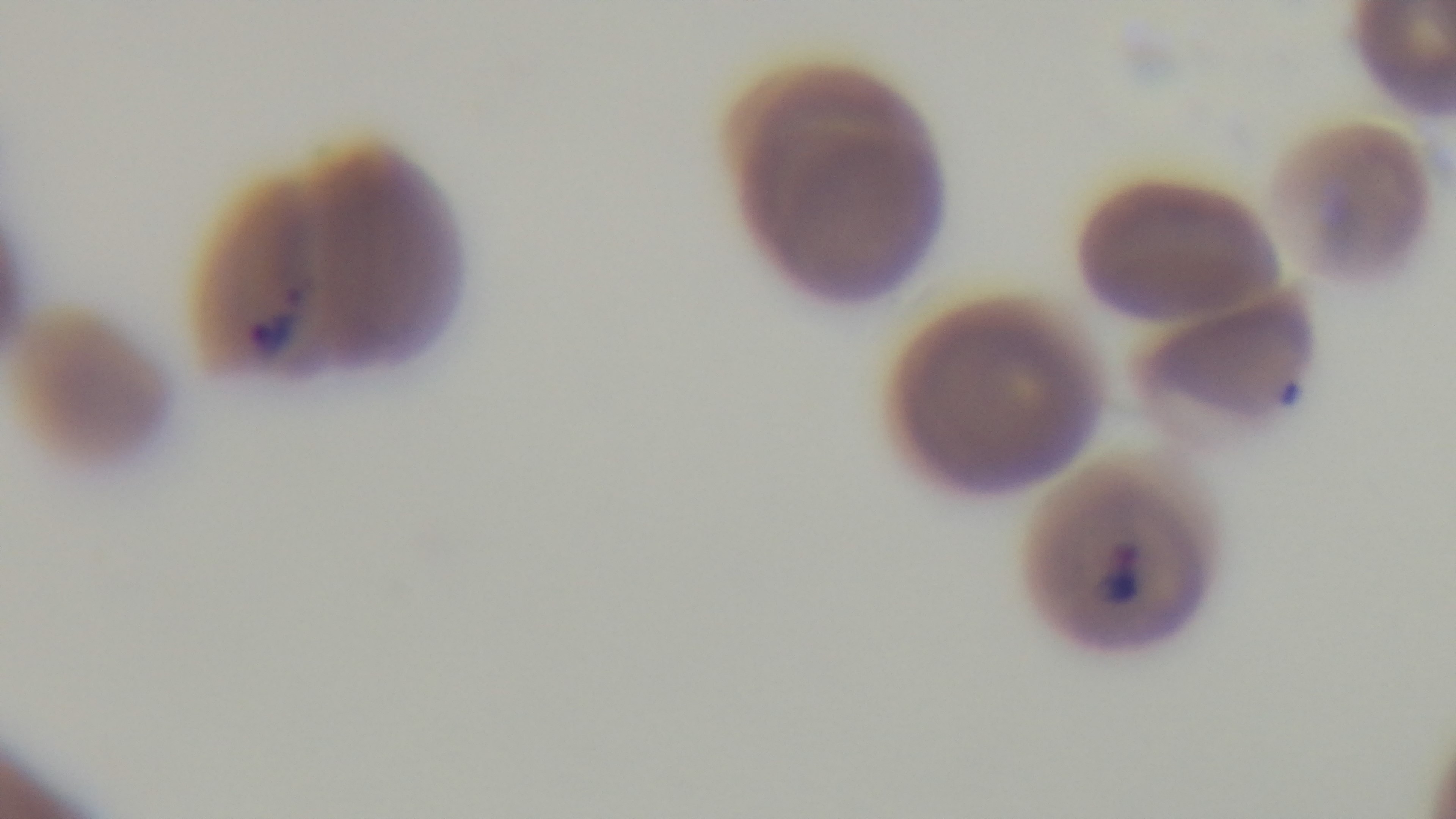
Photomicrograph. Giemsa stain. Preparation: thin. Single field of view. Malaria status: infected. 100x oil-immersion objective. Captured with a mounted 4K digital camera.